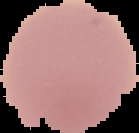
Summary:
  - Result: no Plasmodium parasites detected
  - Preparation: thin blood film
  - Image type: cell region segmented out of the field of view; surrounding area masked to black
  - Image size: 139×133 pixels